Comment on the morphology of the red blood cells.
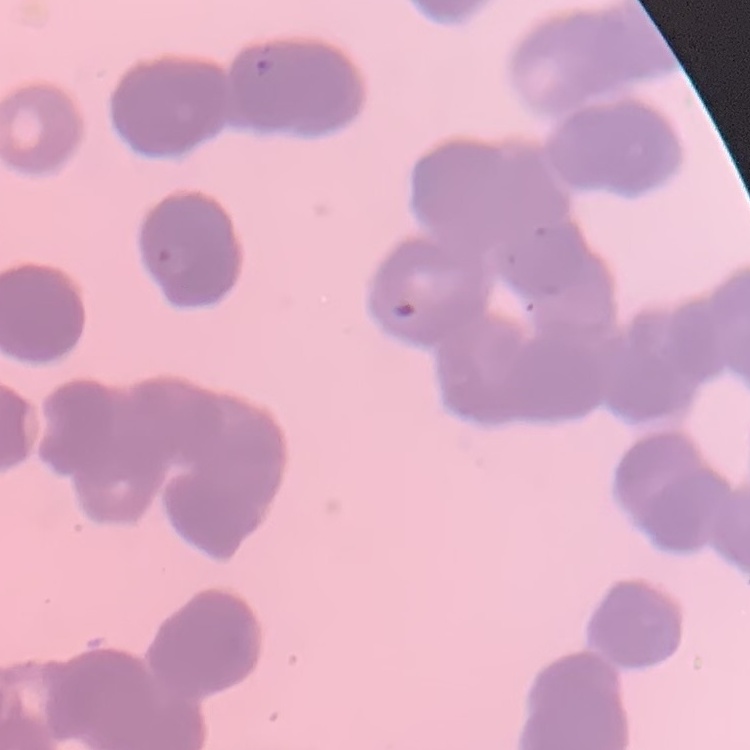
They show rouleaux formation.

Square crop of a larger photomicrograph. Thin blood film. Stained with either Field's or Giemsa.